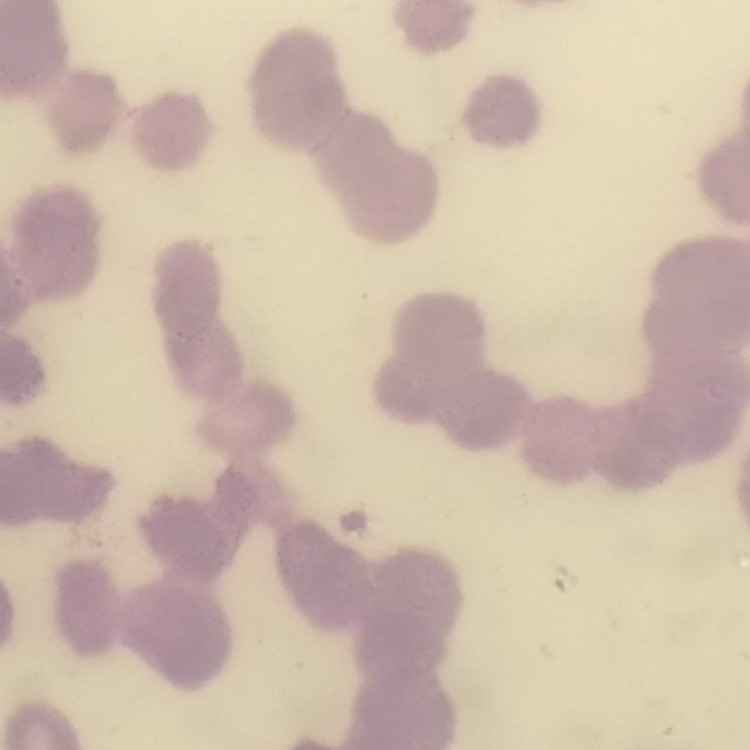

Summary:
  - Erythrocyte morphology: rouleaux formation
  - Preparation: thin peripheral smear
  - Stain: Field's or Giemsa
  - Image type: square crop of a larger photomicrograph